Name the parasite shown.
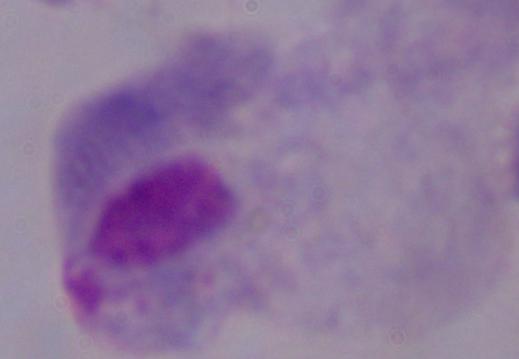

This is a trichomonad.

Summary:
  - Modality: micrograph
  - Magnification: 1000x